Assess the morphology of the red blood cells.
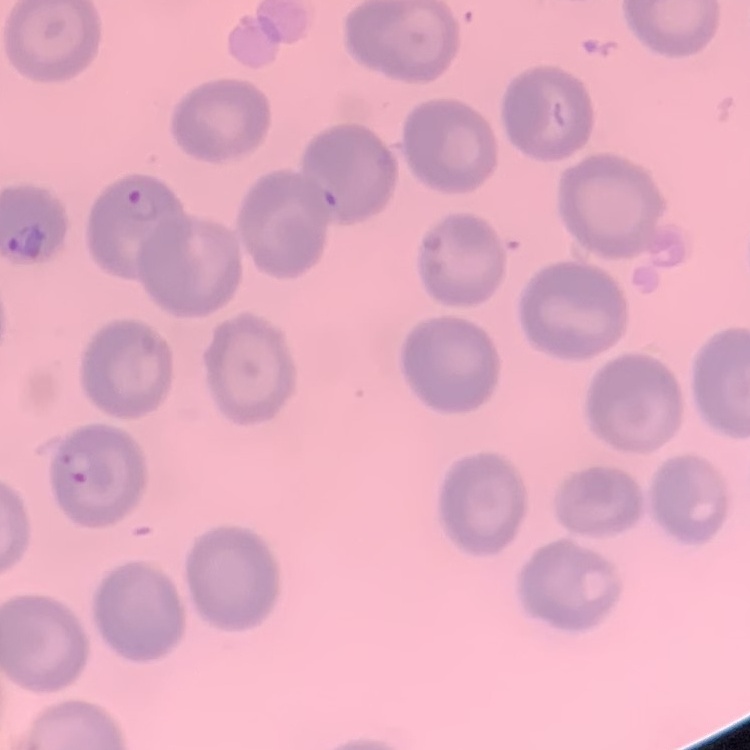
No rouleaux formation.

image type = square crop of a larger photomicrograph
stain = Field's or Giemsa
preparation = thin peripheral smear